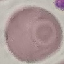
Result: no malaria parasites seen. Giemsa-stained preparation. Thin blood film. Automatically extracted cell patch, resized to 64 × 64 pixels. Acquired by smartphone through the microscope eyepiece.